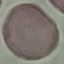
malaria status = uninfected
preparation = thin blood film
image type = cell patch, automatically extracted from a larger field of view and resized to 64 × 64 pixels
capture = smartphone through the microscope eyepiece
stain = Giemsa